Locate every Plasmodium falciparum-infected red blood cell.
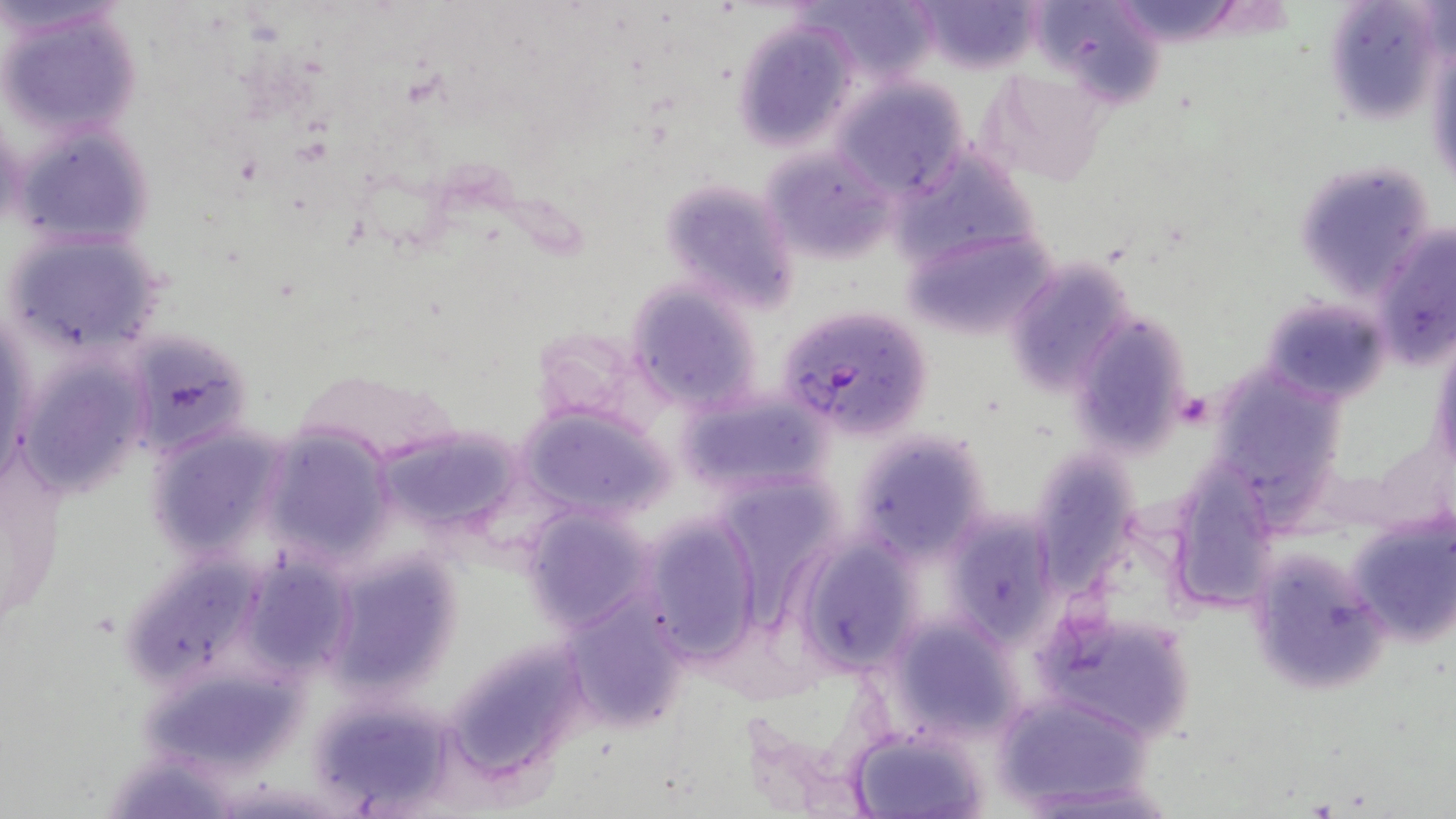
Approximate bounding boxes as named x1/y1/x2/y2 corners in pixels.
Plasmodium falciparum-infected red blood cells: (x1=778, y1=306, x2=934, y2=440).

Uninfected red blood cell locations: (x1=805, y1=0, x2=941, y2=86), (x1=914, y1=0, x2=1044, y2=73), (x1=1106, y1=0, x2=1248, y2=44), (x1=1322, y1=0, x2=1451, y2=124), (x1=1036, y1=1, x2=1168, y2=109), (x1=2, y1=2, x2=145, y2=140), (x1=733, y1=19, x2=858, y2=150), (x1=1428, y1=38, x2=1456, y2=197), (x1=984, y1=70, x2=1114, y2=189), (x1=832, y1=78, x2=968, y2=199), (x1=11, y1=122, x2=159, y2=248), (x1=761, y1=146, x2=893, y2=263), (x1=1295, y1=161, x2=1437, y2=304), (x1=658, y1=176, x2=800, y2=311), (x1=900, y1=222, x2=1057, y2=344), (x1=1372, y1=223, x2=1456, y2=368), (x1=4, y1=230, x2=165, y2=358), (x1=1006, y1=257, x2=1133, y2=395), (x1=626, y1=281, x2=763, y2=412), (x1=1262, y1=293, x2=1392, y2=406), (x1=1067, y1=307, x2=1198, y2=459), (x1=1, y1=309, x2=38, y2=488), (x1=122, y1=328, x2=255, y2=459), (x1=1430, y1=330, x2=1455, y2=483), (x1=16, y1=351, x2=152, y2=498), (x1=1221, y1=363, x2=1345, y2=530), (x1=290, y1=368, x2=460, y2=467), (x1=676, y1=386, x2=832, y2=501), (x1=517, y1=401, x2=671, y2=519), (x1=146, y1=423, x2=290, y2=565), (x1=374, y1=424, x2=528, y2=541), (x1=261, y1=425, x2=398, y2=564), (x1=852, y1=431, x2=990, y2=561), (x1=1030, y1=457, x2=1138, y2=594), (x1=1167, y1=460, x2=1279, y2=611), (x1=520, y1=504, x2=659, y2=632), (x1=940, y1=506, x2=1067, y2=650), (x1=1348, y1=512, x2=1456, y2=648), (x1=643, y1=513, x2=761, y2=663), (x1=794, y1=534, x2=921, y2=674), (x1=1250, y1=546, x2=1389, y2=693), (x1=323, y1=551, x2=464, y2=701), (x1=236, y1=556, x2=358, y2=677), (x1=560, y1=593, x2=689, y2=730), (x1=1035, y1=609, x2=1199, y2=744), (x1=880, y1=610, x2=1027, y2=744), (x1=445, y1=638, x2=591, y2=779), (x1=995, y1=690, x2=1149, y2=808), (x1=305, y1=693, x2=457, y2=812), (x1=848, y1=727, x2=991, y2=818). Slide-level diagnosis: Plasmodium falciparum. May-Grünwald-Giemsa-stained preparation. Image is 1456×819 pixels. Optical microscopy. One field of a larger specimen. 1000x magnification. Thin blood smear.